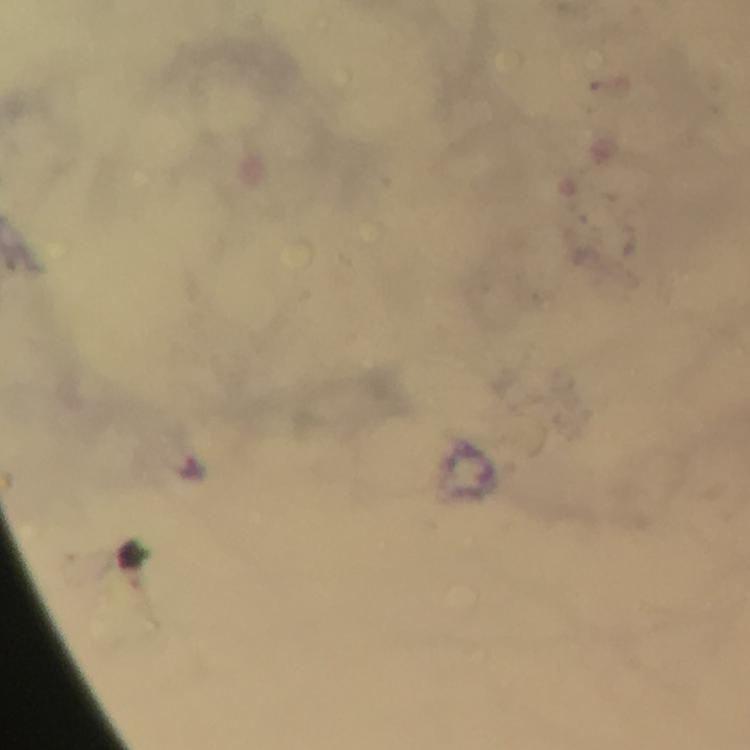 Approximate centers as [x, y] in pixels. Malaria parasite locations: [196, 470]. A crop from one field of view. 100x magnification. Giemsa stain. Immersion oil applied. Photographed with a smartphone mounted on the microscope. From a malaria diagnostic workup. Image is 750×750 pixels. Thick blood film.